Classify this cell by malaria status.
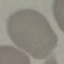

Uninfected.

image_type: cell patch, automatically extracted from a larger field of view and resized to 64 × 64 pixels
preparation: thin blood smear
stain: Giemsa
capture: smartphone through the microscope eyepiece